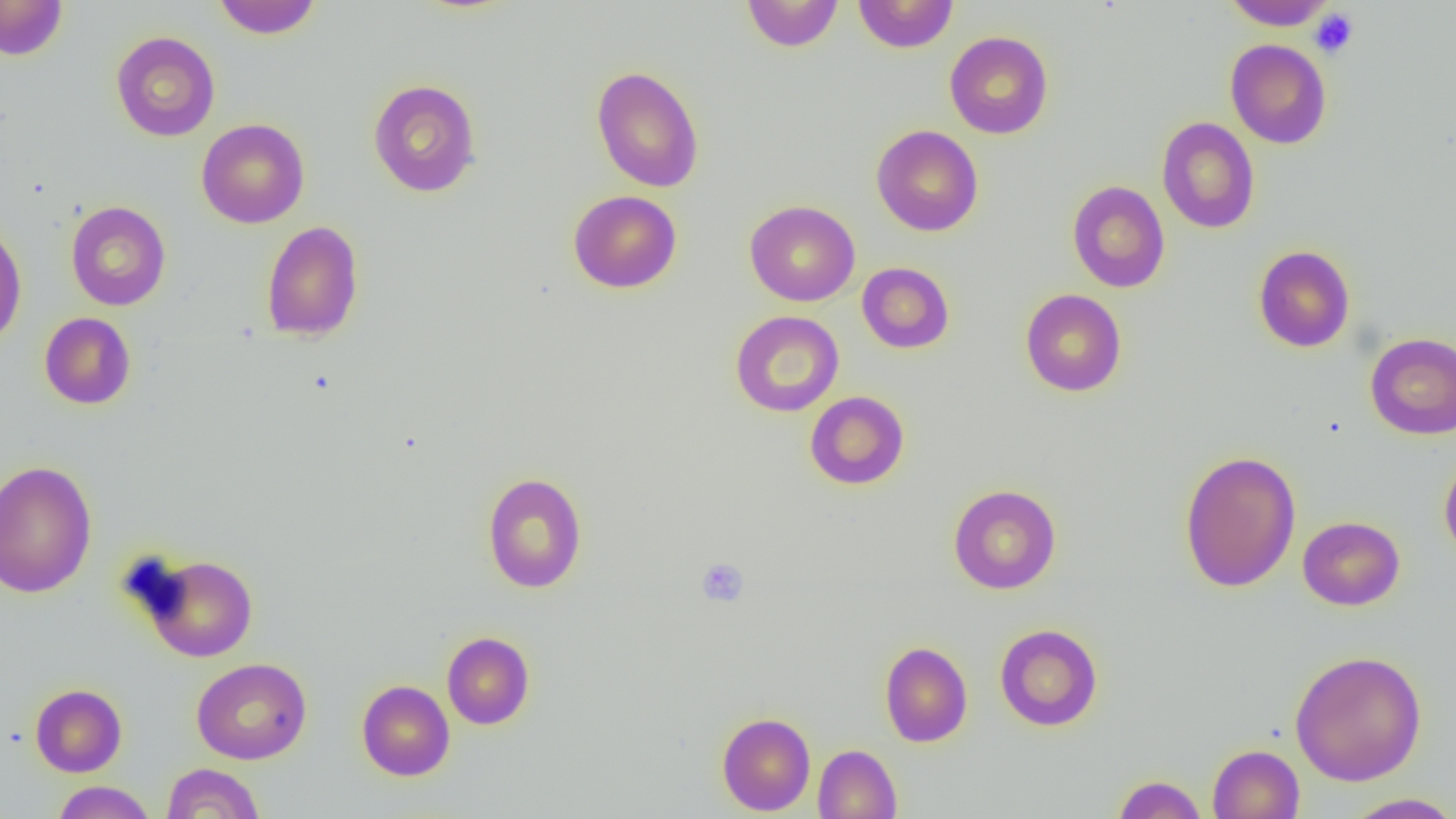

Summary:
  - Coordinate format: approximate bounding boxes as (x1,y1)-(x2,y2) corner pairs in pixels
  - Uninfected red blood cell locations: (0,0)-(68,60), (211,0)-(322,39), (741,0)-(844,52), (852,0)-(959,53), (1223,0)-(1336,30), (110,31)-(220,141), (944,31)-(1053,139), (1225,39)-(1332,149), (591,65)-(704,193), (367,78)-(482,197), (1157,117)-(1259,234), (196,118)-(309,228), (871,124)-(984,237), (1067,179)-(1170,292), (568,190)-(682,293), (744,200)-(860,306), (65,201)-(171,310), (261,220)-(364,342), (0,221)-(27,350), (1253,245)-(1355,353), (857,262)-(954,354), (1020,289)-(1127,397), (730,310)-(844,417), (39,312)-(136,410), (1365,332)-(1456,440), (805,391)-(909,490), (1179,449)-(1302,592), (1439,450)-(1456,564), (0,460)-(98,598), (482,472)-(587,593), (948,484)-(1061,594), (1297,516)-(1405,611), (139,553)-(258,662), (995,623)-(1103,731), (442,631)-(535,730), (879,641)-(973,747), (1289,649)-(1428,786), (191,657)-(312,764), (356,679)-(455,781), (29,684)-(127,776), (716,711)-(816,815), (813,744)-(902,819), (1207,744)-(1305,819), (161,763)-(265,819), (1111,775)-(1207,819), (51,781)-(157,818), (1343,792)-(1456,819)
  - Platelet locations: (1309,9)-(1359,58), (696,557)-(749,607)
  - Slide-level diagnosis: negative for blood parasites
  - Modality: optical microscopy
  - Magnification: 1000x
  - Preparation: thin blood smear
  - Field of view: single
  - Image size: 1456×819 pixels